Give the position of every Plasmodium parasite.
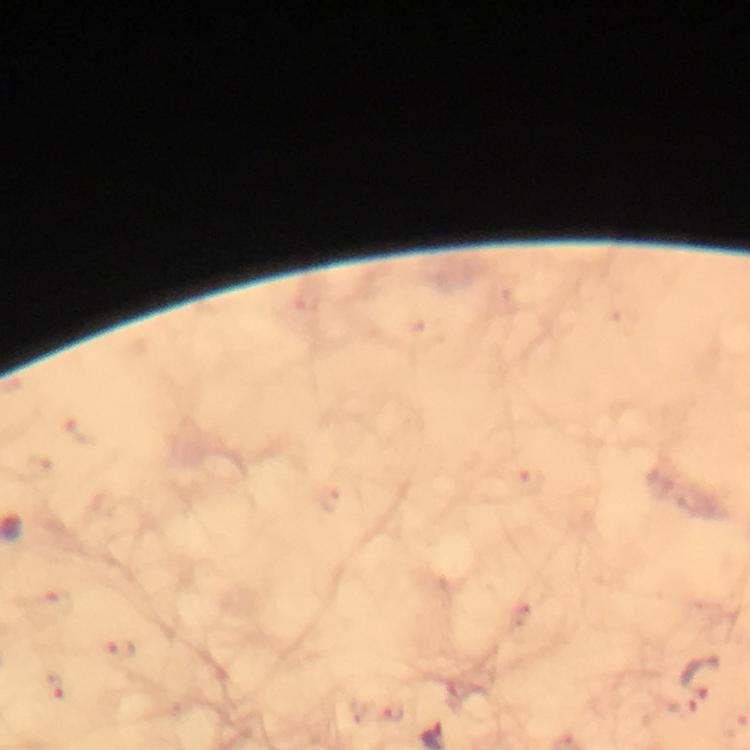
Approximate centers as {x, y} in pixels.
Plasmodium parasites: {58, 601}, {120, 650}, {705, 674}, {55, 686}, {680, 702}, {391, 714}.

Summary:
  - Stain: Giemsa
  - Immersion oil: applied
  - Preparation: thick smear
  - Context: from a malaria diagnostic workup
  - Capture: smartphone mounted on the microscope
  - Cropped from: one field of view
  - Image size: 750×750 pixels
  - Magnification: 100x